Identify the preparation type.
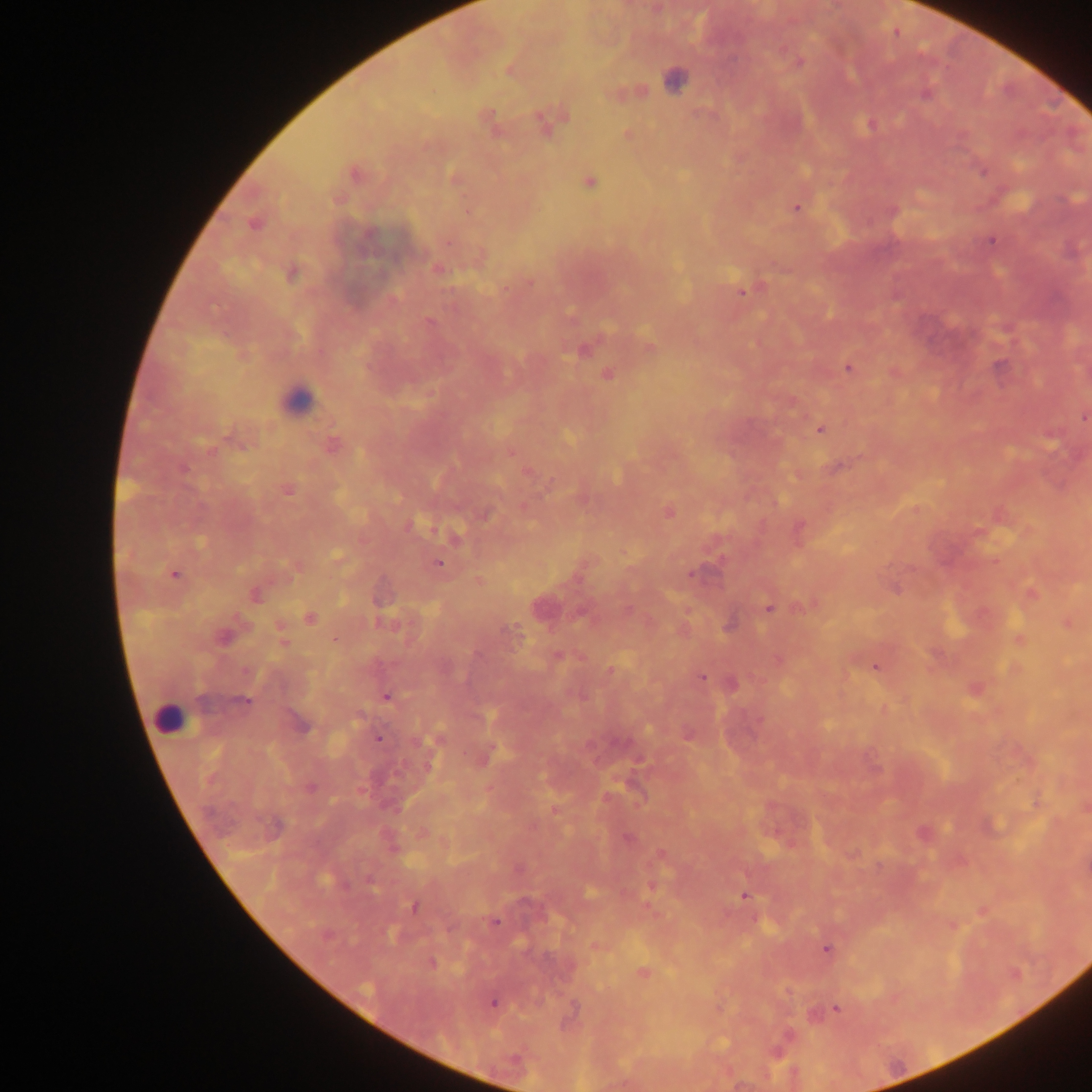

Thick blood film.

image size = 1092×1092 pixels
country = Ghana
capture = mobile-phone photograph through a microscope
leukocyte locations = approximate centers as x y in pixels: 296 401; 168 719
field of view = single
malaria parasite locations = approximate centers as x y in pixels: 655 9; 896 32; 799 62; 509 69; 674 79; 630 92; 925 94; 487 118; 549 119; 870 125; 627 134; 983 170; 354 173; 455 178; 588 181; 796 208; 892 211; 254 222; 992 240; 436 269; 292 272; 529 282; 743 289; 429 322; 650 346; 584 349; 849 367; 607 373; 895 373; 1083 416; 820 429; 238 438; 331 445; 527 472; 287 489; 583 499; 669 511; 484 515; 799 528; 438 563; 295 566; 174 574; 478 580; 1030 592; 255 595; 811 604; 541 607; 769 607; 310 617; 1066 623; 280 627; 511 632; 222 636; 335 640; 1019 640; 558 655; 778 660; 876 666; 611 671; 702 676; 731 683; 975 688; 386 697; 243 702; 300 724; 687 734; 377 738; 436 740; 484 757; 1037 802; 1085 807; 554 809; 923 834; 627 837; 661 855; 651 885; 744 894; 414 907; 982 910; 494 921; 952 924; 596 946; 827 948; 431 963; 642 973; 494 1002; 836 1007; 574 1008